Locate and identify every blood parasite.
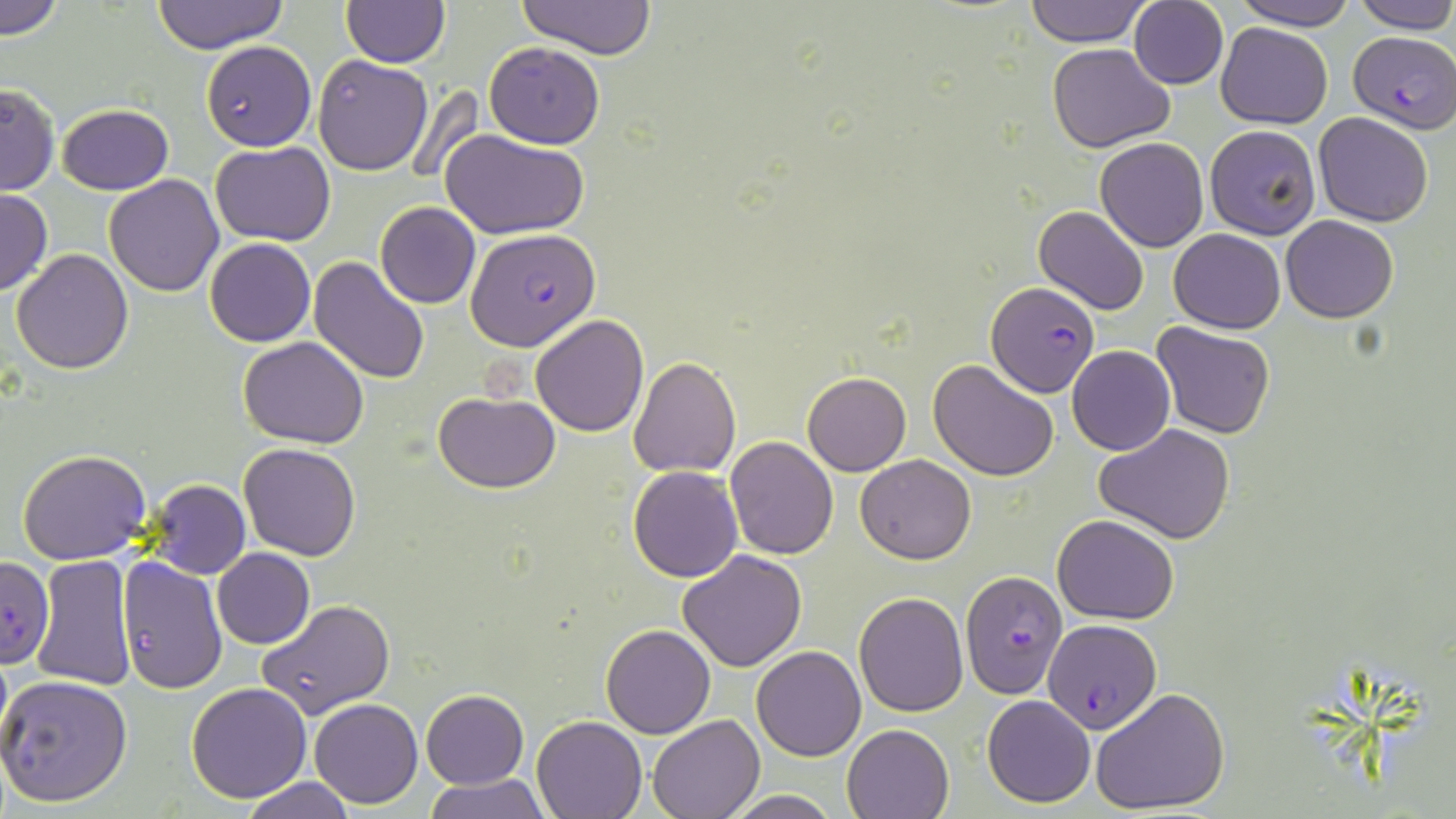
Approximate bounding boxes as [x1, y1, x2, y2] in pixels.
Plasmodium falciparum-infected red blood cells: [1349, 30, 1456, 132], [466, 228, 600, 351], [986, 282, 1100, 397], [1, 557, 54, 668], [959, 569, 1069, 699], [1044, 619, 1161, 732].
No Plasmodium ovale, Plasmodium malariae, Plasmodium vivax, Babesia divergens, or Trypanosoma brucei observed.

Uninfected red blood cell locations: [0, 0, 65, 38], [149, 0, 290, 53], [1025, 0, 1152, 46], [1230, 0, 1359, 30], [1350, 0, 1456, 32], [517, 1, 659, 58], [342, 2, 449, 67], [1129, 2, 1228, 88], [1215, 23, 1333, 129], [201, 39, 316, 151], [483, 42, 606, 148], [1046, 42, 1175, 151], [312, 54, 433, 174], [1, 83, 59, 197], [58, 103, 173, 194], [1314, 112, 1434, 227], [1204, 125, 1321, 240], [443, 130, 590, 241], [1095, 137, 1208, 253], [211, 140, 335, 245], [103, 175, 226, 295], [0, 189, 52, 296], [375, 202, 481, 309], [1033, 205, 1149, 316], [1281, 215, 1398, 323], [1168, 228, 1285, 333], [205, 238, 316, 348], [10, 249, 133, 373], [310, 258, 430, 387], [531, 315, 649, 437], [1152, 324, 1275, 439], [238, 336, 369, 449], [1067, 346, 1175, 455], [629, 356, 742, 478], [929, 359, 1059, 481], [803, 372, 911, 475], [433, 392, 559, 492], [1095, 422, 1237, 545], [724, 435, 839, 560], [239, 443, 362, 561], [17, 448, 152, 565], [856, 454, 976, 565], [628, 466, 744, 583], [144, 479, 250, 580], [1051, 514, 1180, 623], [212, 547, 314, 648], [678, 551, 808, 671], [116, 554, 227, 694], [29, 555, 137, 691], [855, 591, 969, 717], [257, 599, 395, 720], [601, 624, 715, 737], [752, 646, 866, 762], [0, 674, 132, 807], [187, 683, 312, 803], [1090, 687, 1229, 814], [420, 690, 529, 789], [983, 695, 1096, 807], [310, 697, 422, 808], [532, 714, 647, 817], [647, 714, 763, 819], [841, 723, 953, 819], [426, 773, 551, 819], [239, 777, 358, 819], [724, 790, 841, 819]. Slide-level diagnosis: Plasmodium falciparum. May-Grünwald-Giemsa-stained preparation. Thin blood smear. One field of a larger specimen. Optical microscopy. 1000x magnification. Image is 1456×819 pixels.